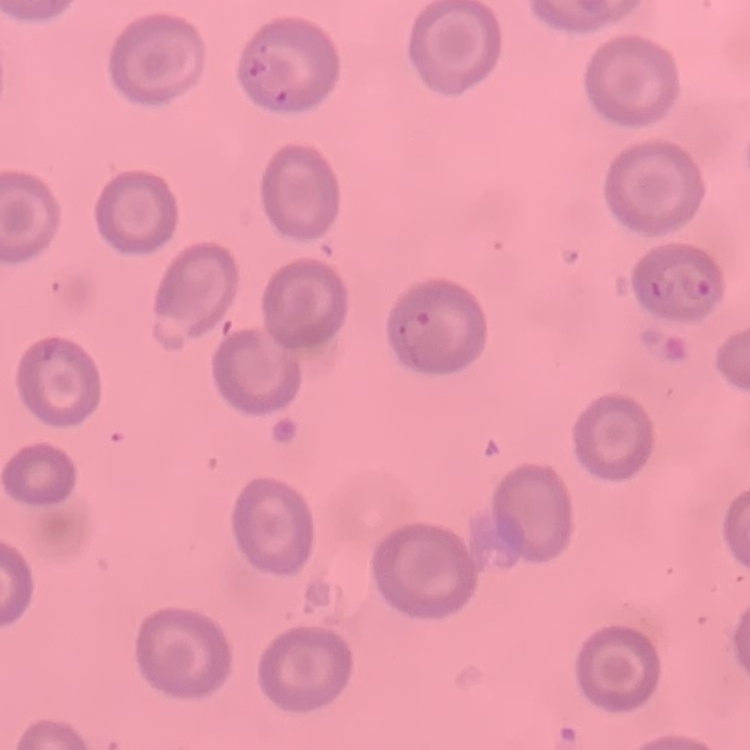
The red blood cells show no rouleaux formation. Thin blood film. Stained with either Field's or Giemsa. Square crop of a larger photomicrograph.